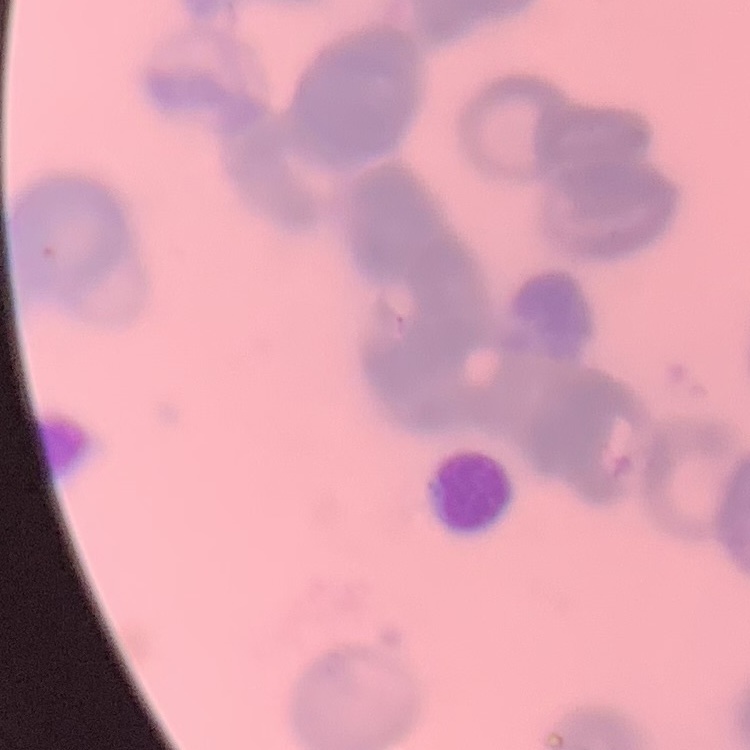
red blood cell morphology = rouleaux formation
image type = one tile cut from a larger photomicrograph
stain = Field's or Giemsa
preparation = thin blood smear